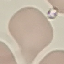

malaria status = uninfected
preparation = thin blood smear
capture = smartphone through the microscope eyepiece
image type = cell patch, automatically extracted from a larger field of view and resized to 64 × 64 pixels
stain = Giemsa